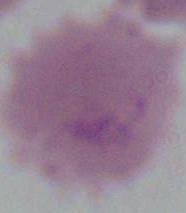

An erythrocyte is shown. Micrograph. 1000x magnification.